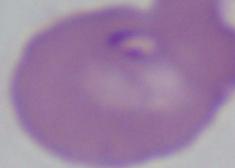
identification = Babesia
modality = micrograph
magnification = 1000x